Outline each blood parasite and name the species.
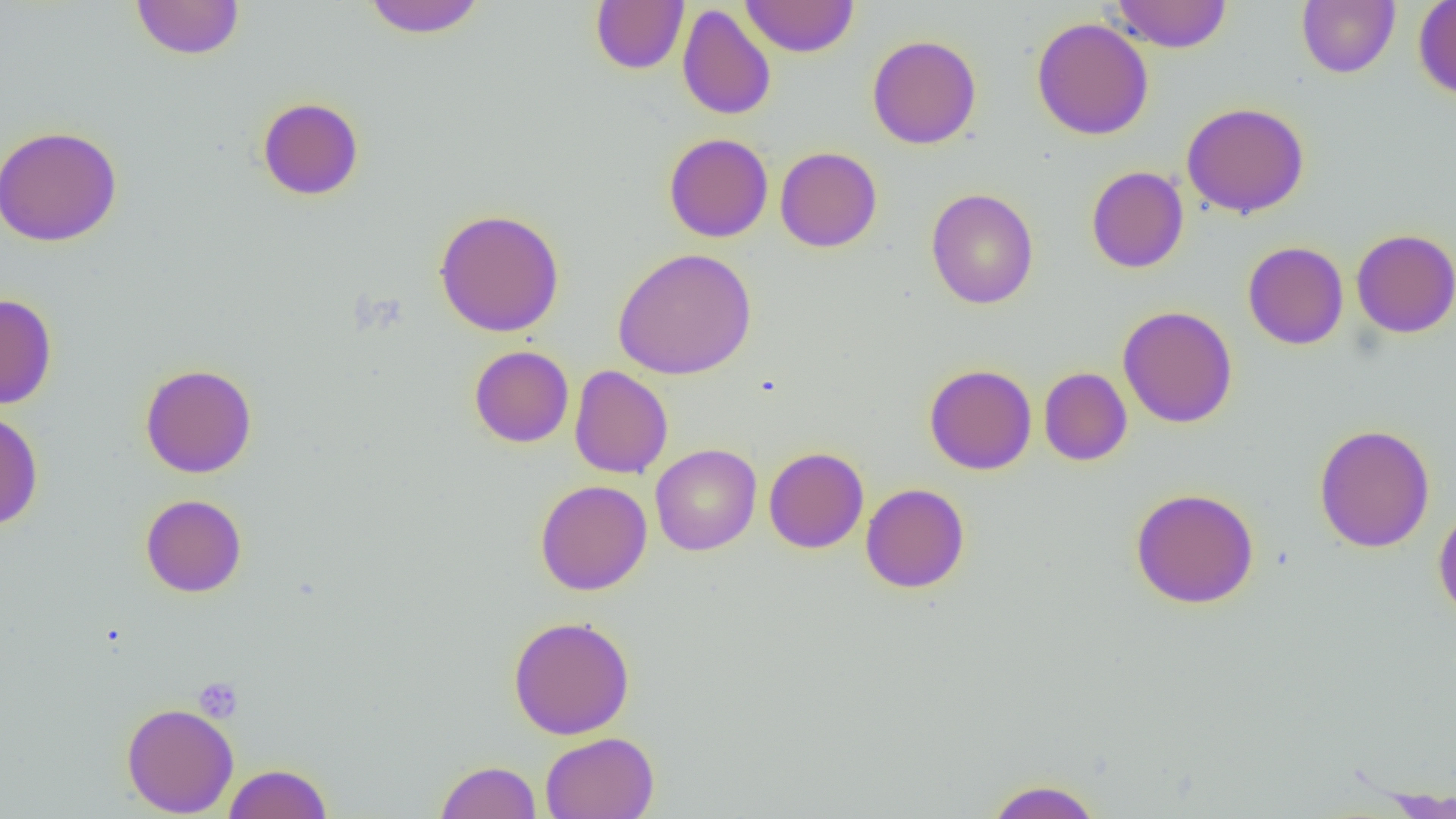

No blood parasites observed.

Approximate bounding boxes as [x1, y1, x2, y2] in pixels. Platelet locations: [193, 677, 242, 723]. Uninfected red blood cell locations: [130, 0, 245, 60], [361, 0, 487, 38], [591, 0, 689, 74], [740, 0, 859, 57], [1111, 0, 1232, 53], [1296, 0, 1400, 78], [1413, 0, 1456, 100], [677, 5, 776, 120], [1031, 17, 1154, 140], [867, 34, 982, 149], [257, 97, 364, 201], [1181, 102, 1310, 219], [0, 125, 123, 247], [663, 133, 773, 242], [775, 147, 882, 252], [1086, 166, 1189, 273], [925, 188, 1039, 309], [434, 208, 565, 337], [1351, 229, 1456, 338], [1242, 241, 1349, 350], [612, 247, 758, 380], [0, 293, 57, 409], [1118, 305, 1238, 428], [469, 345, 574, 448], [140, 363, 257, 478], [924, 364, 1037, 475], [569, 365, 673, 479], [1039, 367, 1132, 466], [0, 410, 44, 530], [1314, 424, 1435, 553], [650, 444, 761, 555], [763, 447, 869, 553], [535, 479, 652, 595], [860, 483, 970, 594], [1130, 487, 1259, 609], [140, 494, 247, 597], [1433, 504, 1456, 623], [507, 615, 636, 740], [121, 702, 238, 817], [540, 731, 659, 818], [434, 760, 542, 819], [222, 763, 333, 819], [985, 778, 1102, 818]. Slide-level diagnosis: negative for blood parasites. 1000x magnification. One field of a larger specimen. Image is 1456×819 pixels. Optical microscopy. Thin blood smear.